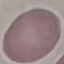
result = no malaria parasites detected
stain = Giemsa
image type = cell patch, automatically extracted from a larger field of view and resized to 64 × 64 pixels
capture = smartphone through the microscope eyepiece
preparation = thin blood film